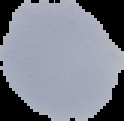

{
  "malaria_status": "uninfected",
  "image_type": "cell region segmented out of the field of view; surrounding area masked to black",
  "preparation": "thin blood smear",
  "image_size": "124×121 pixels"
}